Classify this cell by malaria status.
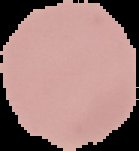

It is uninfected.

{
  "preparation": "thin blood film",
  "image_type": "segmented cell region with the area outside set to black",
  "image_size": "139×151 pixels"
}